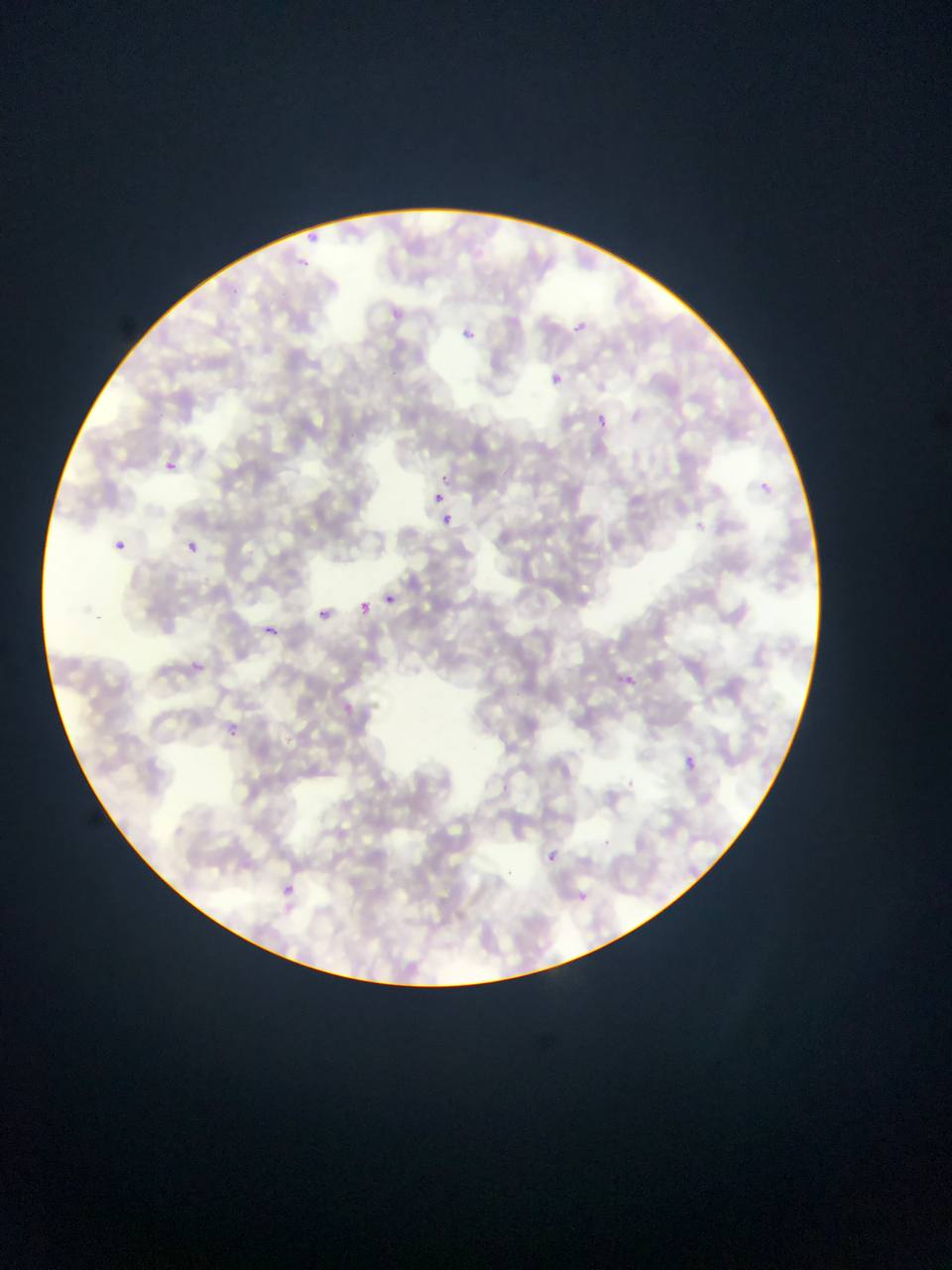

Approximate bounding boxes as left top right bottom in pixels. Malaria parasite locations: 304 232 319 243; 296 251 325 283; 383 301 419 329; 567 301 599 337; 455 320 486 359; 545 367 572 393; 577 406 633 440; 166 461 177 471; 435 462 450 488; 755 467 792 511; 435 491 446 503; 436 511 460 537; 689 514 718 539; 114 539 127 551; 186 541 198 553; 384 594 396 605; 359 602 372 616; 319 609 330 618; 264 625 277 635; 193 647 218 684; 615 665 653 703; 225 720 250 752; 684 756 697 770; 538 838 559 860; 278 871 318 927; 575 879 585 899. Collected in Ghana. Image is 952×1270 pixels. Thin blood smear. One field of view. Mobile-phone photograph taken through the microscope.